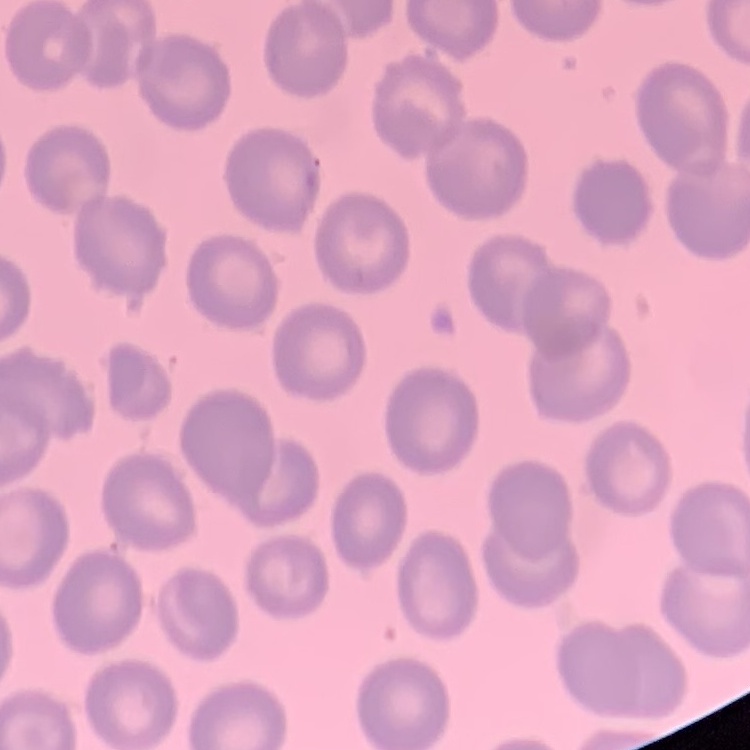

erythrocyte morphology = no rouleaux formation
stain = Field's or Giemsa
preparation = thin blood film
image type = square crop of a larger photomicrograph